Classify this cell by malaria status.
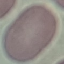

Uninfected.

Thin blood film. Cell patch, automatically extracted from a larger field of view and resized to 64 × 64 pixels. Giemsa-stained preparation. Acquired by smartphone through the microscope eyepiece.